Give a bounding box for every leukocyte visible.
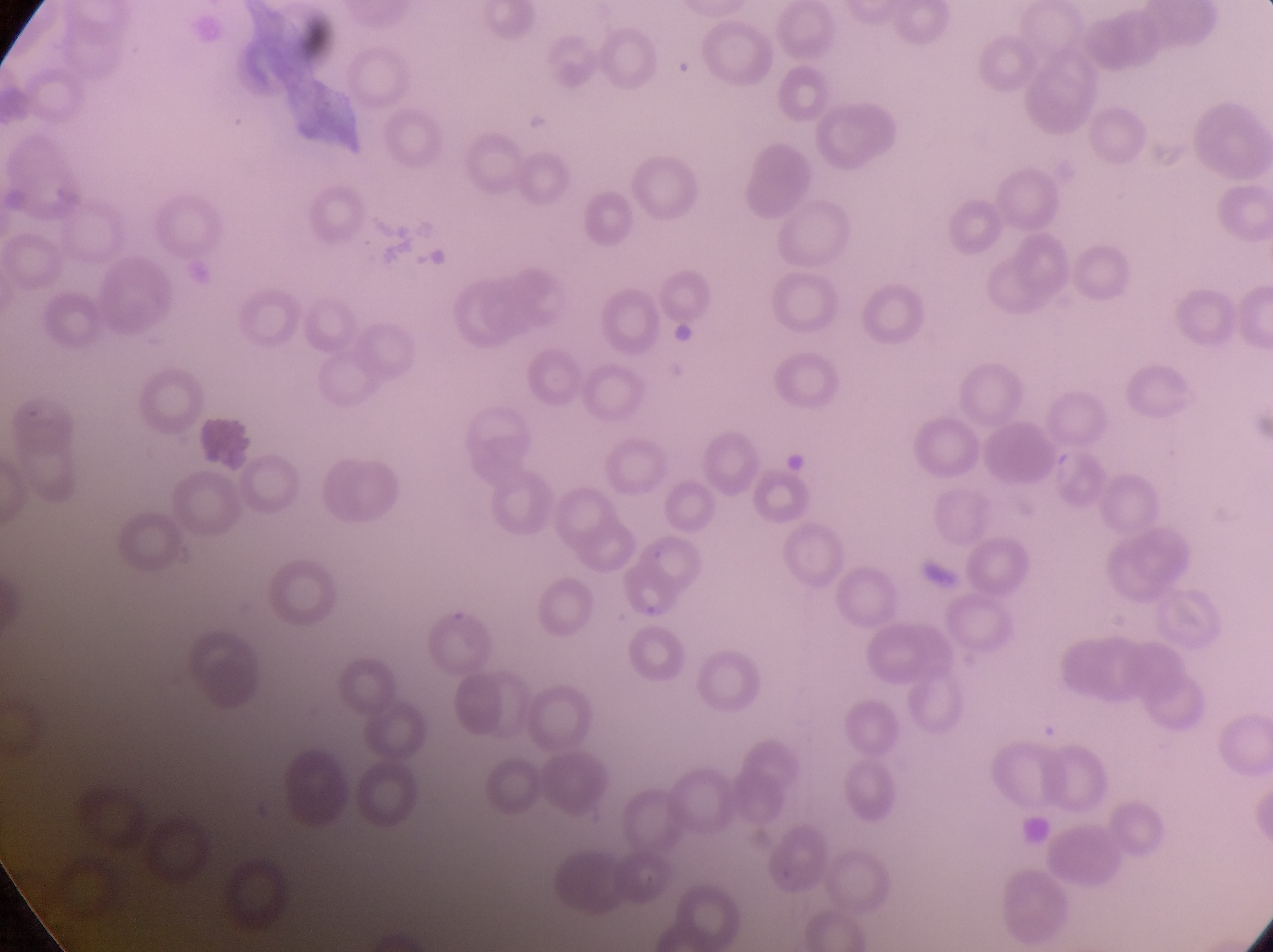

Approximate bounding boxes as left top right bottom in pixels.
Leukocytes: 196 416 254 473.

Summary:
  - Parasitised red blood cell locations: 612 554 689 621
  - Artifact (platelet-like body, stain precipitate, or debris) locations: 286 8 338 66; 786 450 812 474; 918 553 959 589
  - Preparation: thin blood smear
  - Country: Uganda
  - Capture: smartphone photograph through the eyepiece of an Olympus CX-23 microscope
  - Field of view: single
  - Image size: 1273×952 pixels
  - Magnification: 1000x